Classify this cell by malaria status.
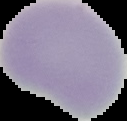

Uninfected.

Segmented cell region on a black background. Image is 127×121 pixels. From a thin blood film.